Assess the morphology of the erythrocytes.
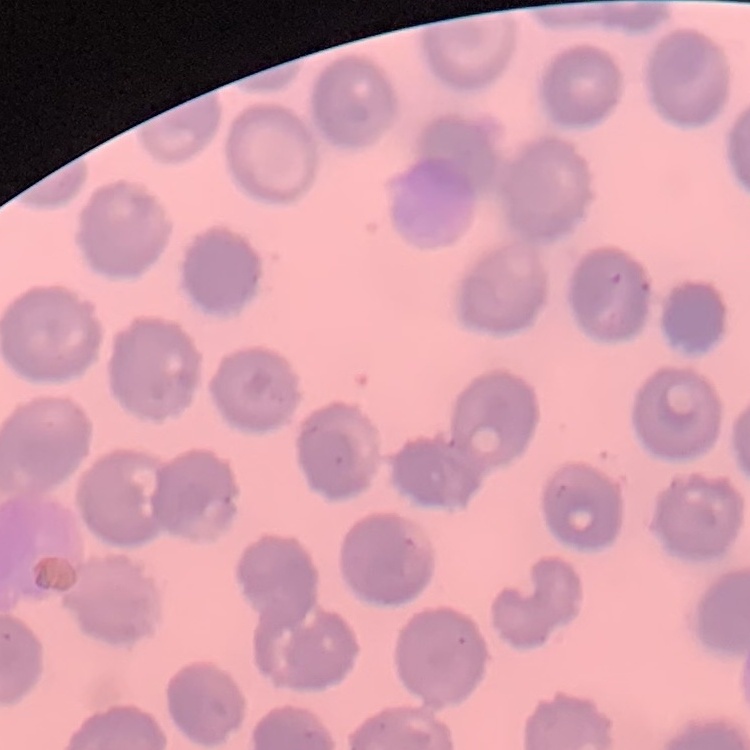

They show no rouleaux formation.

Summary:
  - Stain: Field's or Giemsa
  - Image type: square crop of a larger photomicrograph
  - Preparation: thin blood smear